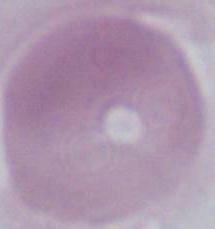
Photomicrograph. 1000x magnification. An erythrocyte is shown.